Give the position of every Plasmodium parasite and every leukocyte.
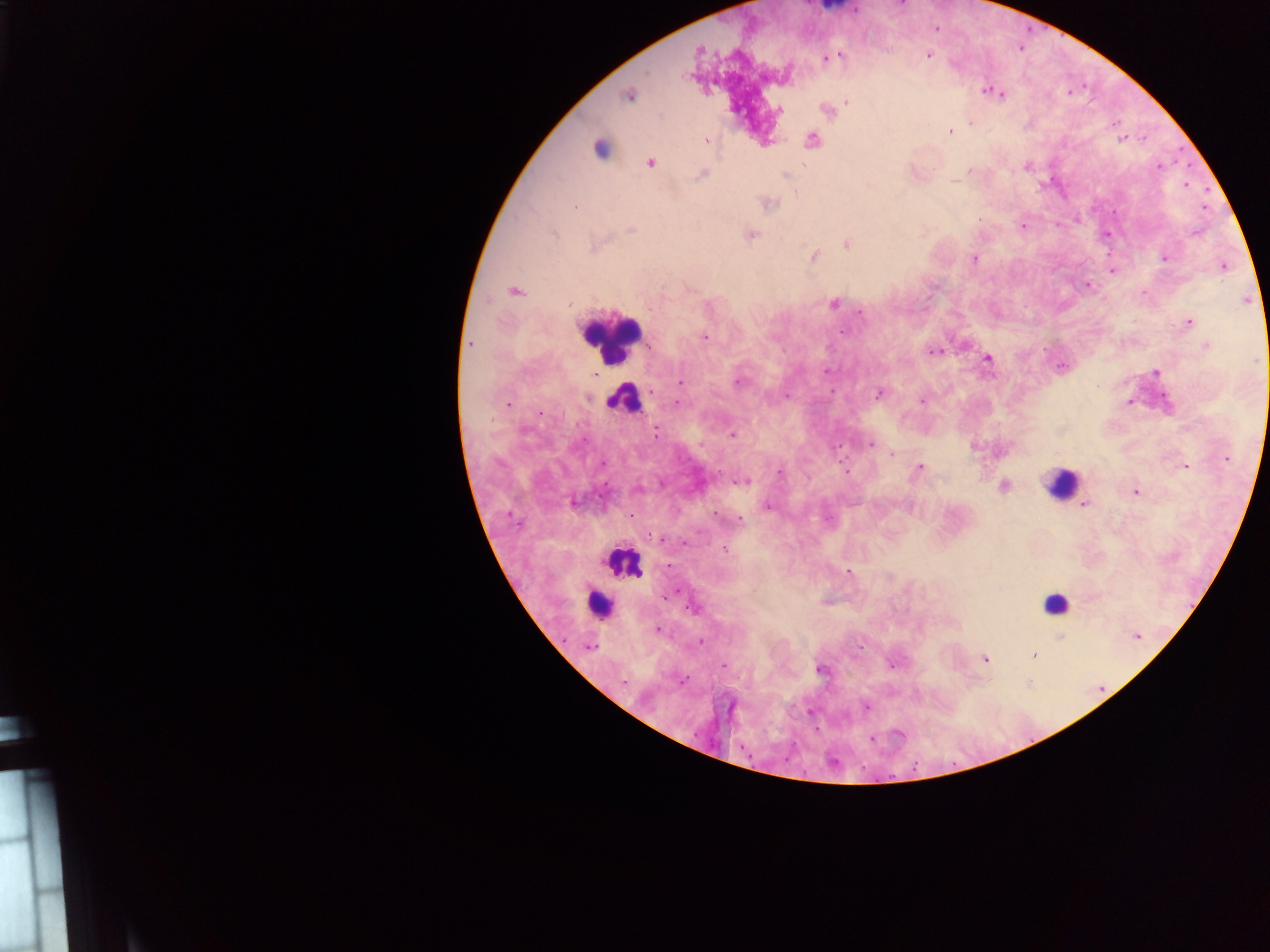

Approximate centers as (x, y) in pixels.
Plasmodium parasites: (839, 54), (928, 54), (829, 57), (822, 58), (991, 91), (998, 92), (628, 95), (847, 102), (778, 109), (826, 109), (971, 121), (1114, 122), (949, 131), (1123, 138), (1143, 138), (812, 140), (705, 141), (600, 148), (650, 163), (1026, 166), (1158, 166), (970, 169), (702, 174), (785, 174), (1185, 184), (795, 193), (767, 203), (575, 206), (1203, 207), (1022, 226), (1196, 232), (749, 234), (1106, 234), (847, 243), (813, 256), (974, 257), (1164, 257), (1223, 265), (1112, 270), (1087, 284), (514, 290), (1246, 299), (834, 303), (859, 312), (1187, 322), (843, 331), (705, 337), (470, 344), (1206, 346), (935, 352), (988, 359), (1060, 367), (827, 371), (1155, 372), (738, 381), (680, 382), (879, 394), (786, 395), (922, 399), (677, 401), (1129, 401), (507, 404), (655, 430), (732, 434), (870, 444), (972, 446), (891, 453), (1227, 458), (601, 464), (1186, 467), (919, 468), (779, 471), (741, 481), (1003, 486), (637, 489), (1135, 491), (573, 500), (1084, 504), (767, 505), (631, 516), (739, 520), (662, 539), (684, 541), (669, 566), (848, 571), (664, 594), (692, 607), (657, 629), (1137, 635), (1060, 640), (700, 641), (589, 646), (1034, 655), (984, 659), (893, 663), (724, 664), (821, 668), (681, 680), (1028, 683), (866, 707), (810, 712), (815, 729), (899, 732), (871, 740).
Leukocytes: (609, 336), (624, 399), (1060, 483), (622, 561), (598, 603), (1055, 603).

Summary:
  - Preparation: thick blood film
  - Image size: 1270×952 pixels
  - Capture: mobile-phone photograph through a microscope
  - Field of view: single
  - Country: Ghana